Describe the morphology of the red blood cells.
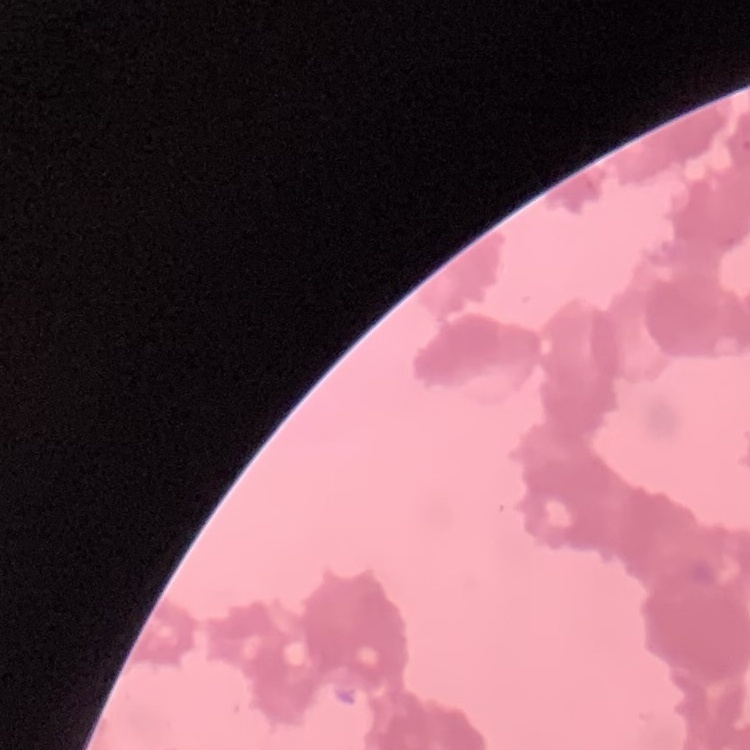

Rouleaux formation.

preparation = thin peripheral smear
image type = square crop of a larger photomicrograph
stain = Field's or Giemsa